Assess this cell for malaria.
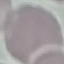
It is uninfected.

capture = smartphone through the microscope eyepiece
stain = Giemsa
image type = automatically extracted cell patch, resized to 64 × 64 pixels
preparation = thin blood film